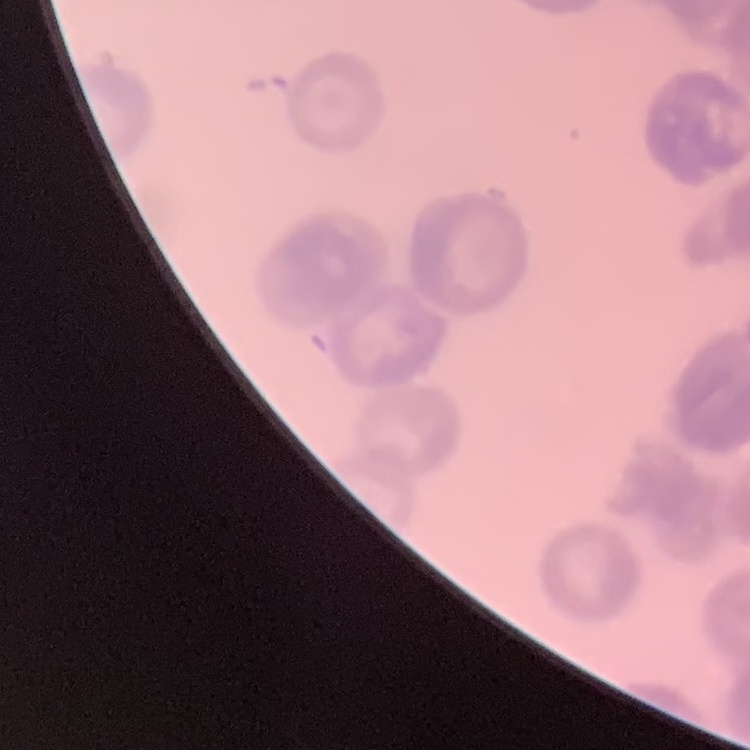
{
  "red_blood_cell_morphology": "rouleaux formation",
  "preparation": "thin blood smear",
  "stain": "Field's or Giemsa",
  "image_type": "one tile cut from a larger photomicrograph"
}